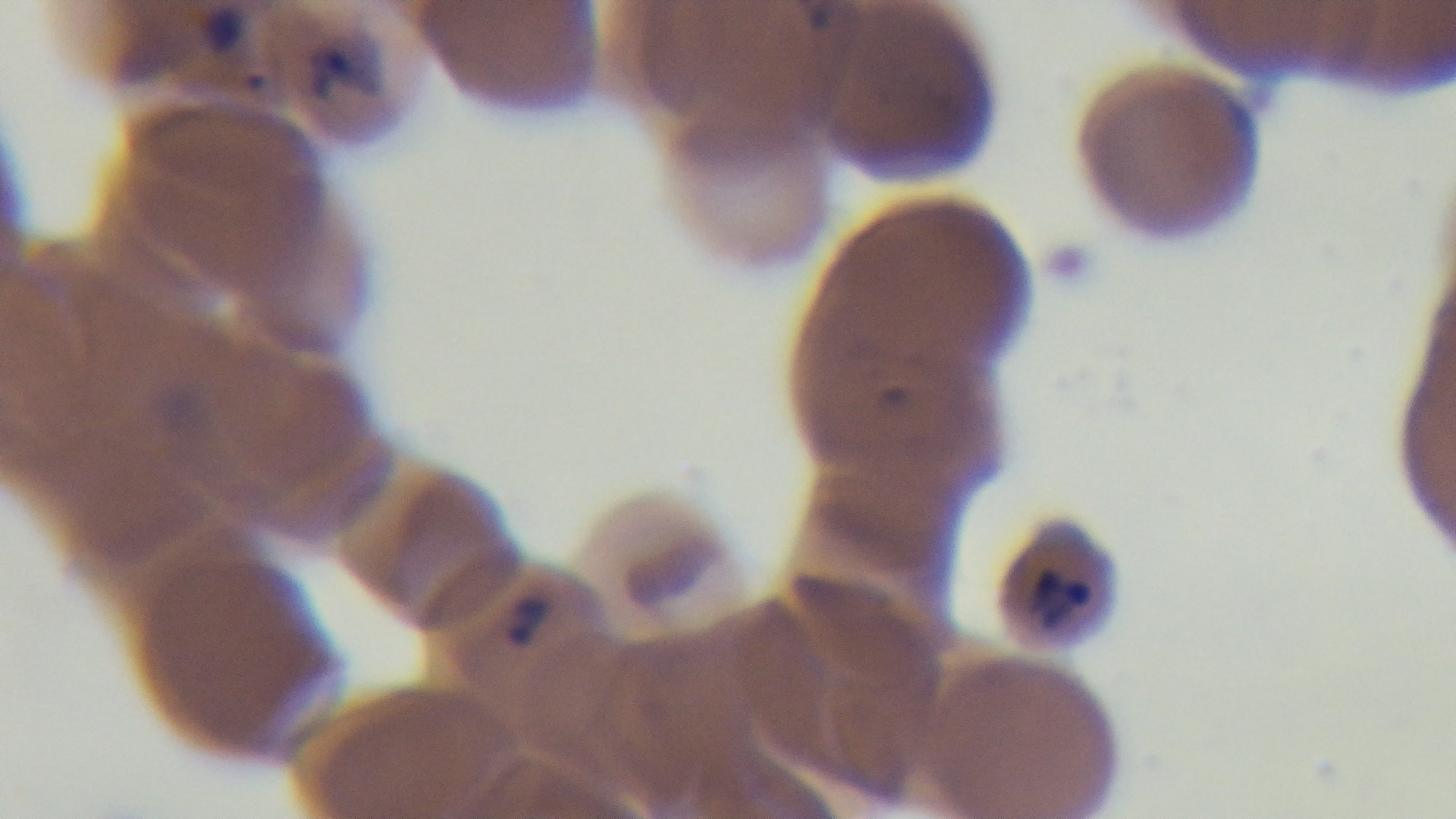

field of view = single
capture = mounted 4K digital camera
stain = Giemsa
objective = 100x oil immersion
malaria status = infected
modality = light microscopy
preparation = thin smear